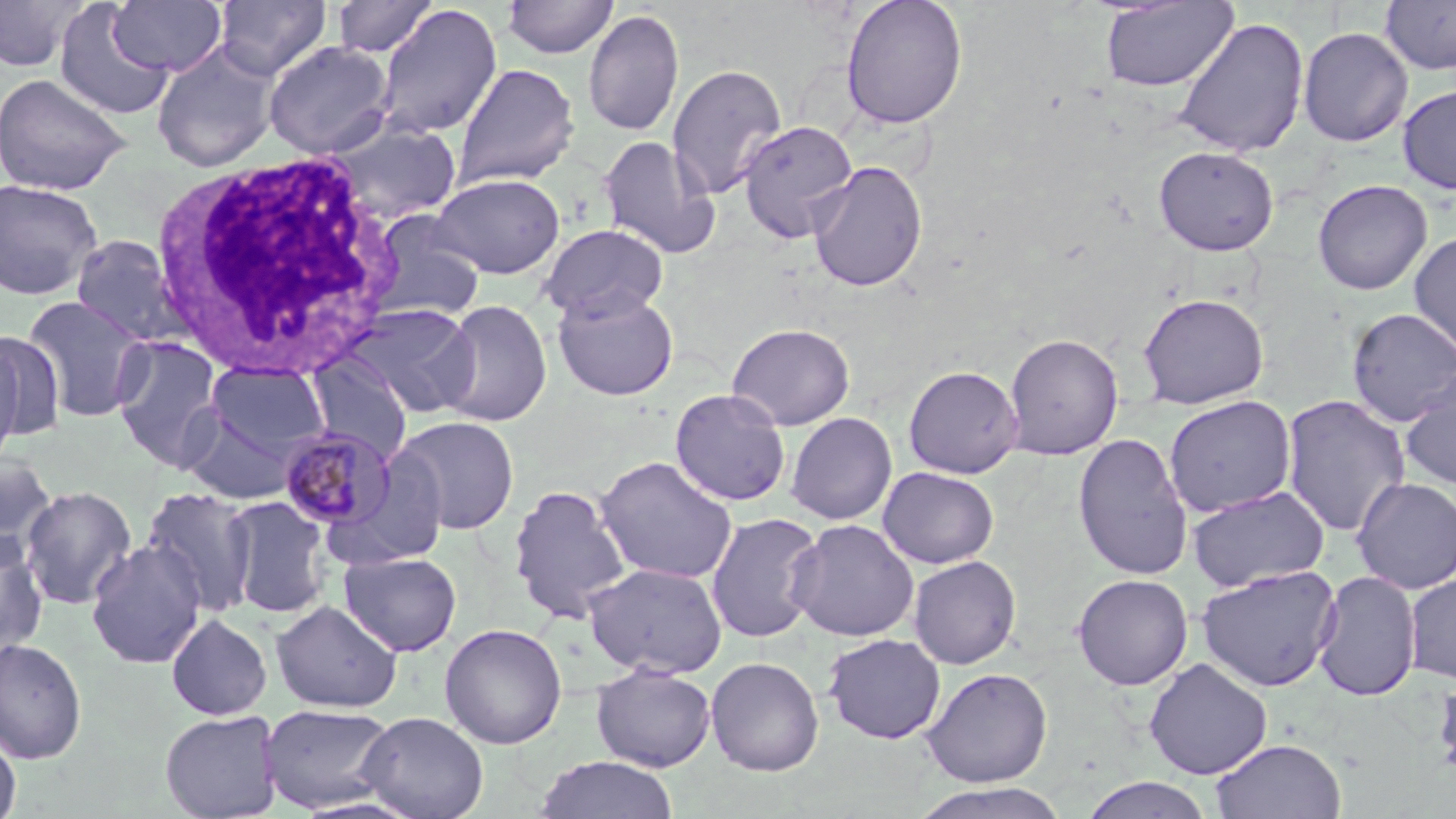
Approximate bounding boxes as (x1, y1, x2, y2) in pixels. Uninfected red blood cell locations: (0, 0, 90, 72), (108, 0, 227, 76), (215, 0, 331, 80), (332, 0, 438, 58), (502, 0, 619, 59), (840, 0, 968, 130), (1099, 1, 1238, 92), (1380, 1, 1456, 75), (53, 3, 175, 120), (374, 4, 502, 139), (583, 9, 684, 137), (1173, 16, 1310, 157), (1298, 26, 1413, 147), (263, 40, 394, 159), (151, 41, 282, 172), (452, 62, 580, 189), (667, 63, 788, 201), (0, 72, 131, 196), (1397, 84, 1456, 195), (737, 119, 858, 243), (327, 120, 462, 225), (597, 135, 722, 260), (1153, 145, 1279, 256), (807, 161, 928, 293), (429, 172, 565, 279), (0, 179, 103, 300), (1312, 179, 1433, 295), (365, 210, 485, 323), (538, 223, 668, 323), (1409, 231, 1456, 363), (70, 235, 185, 347), (552, 288, 679, 401), (1137, 292, 1270, 410), (21, 294, 152, 422), (437, 299, 552, 427), (341, 303, 481, 417), (1346, 308, 1456, 427), (726, 322, 855, 430), (1, 328, 64, 447), (1003, 333, 1124, 460), (112, 335, 224, 470), (0, 336, 27, 472), (304, 355, 413, 464), (206, 361, 330, 458), (903, 365, 1024, 478), (1399, 369, 1456, 491), (669, 388, 791, 506), (1280, 393, 1412, 537), (1163, 395, 1297, 518), (181, 408, 298, 504), (785, 412, 897, 525), (394, 415, 520, 535), (1072, 432, 1195, 580), (0, 453, 58, 566), (333, 453, 452, 569), (595, 455, 738, 584), (878, 466, 999, 568), (1351, 477, 1456, 595), (508, 484, 631, 623), (19, 486, 138, 610), (141, 486, 259, 616), (1186, 486, 1330, 593), (223, 496, 332, 618), (705, 512, 826, 643), (786, 518, 919, 642), (0, 534, 48, 658), (86, 540, 207, 669), (339, 552, 462, 657), (908, 555, 1021, 669), (584, 562, 728, 678), (1196, 565, 1341, 691), (1313, 570, 1422, 702), (1404, 572, 1456, 684), (1072, 573, 1193, 690), (271, 599, 402, 713), (166, 613, 272, 720), (439, 622, 567, 749), (823, 633, 946, 744), (0, 638, 87, 764), (705, 656, 825, 776), (1144, 658, 1273, 779), (591, 664, 716, 772), (921, 667, 1053, 787), (1432, 667, 1456, 785), (259, 702, 398, 814), (160, 709, 283, 819), (357, 711, 489, 819), (0, 728, 22, 819), (1211, 738, 1346, 819), (533, 755, 680, 818), (1079, 776, 1215, 819), (910, 781, 1071, 819). Plasmodium malariae-infected red blood cell locations: (279, 427, 394, 529). White blood cell locations: (150, 149, 406, 376). Slide-level diagnosis: Plasmodium malariae. 1000x magnification. Optical microscopy. May-Grünwald-Giemsa stain. One field of a larger specimen. Thin blood film. Image is 1456×819 pixels.